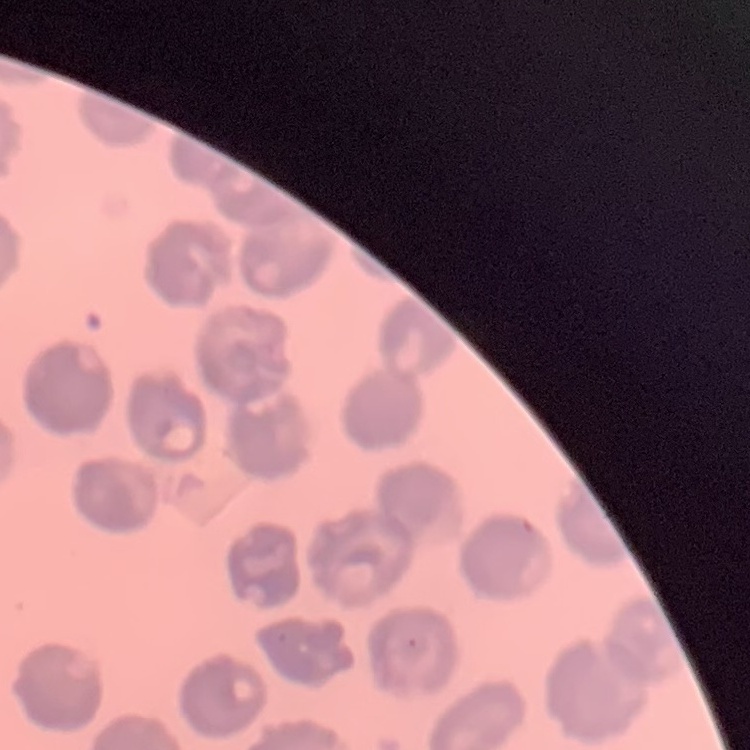
red blood cell morphology = no rouleaux formation
preparation = thin peripheral smear
stain = Field's or Giemsa
image type = square crop of a larger photomicrograph